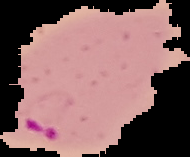
Summary:
  - Preparation: thin blood smear
  - Image type: segmented cell region on a black background
  - Image size: 190×157 pixels
  - Malaria status: parasitized